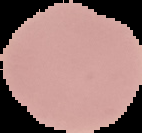 Result: no Plasmodium parasites seen. Segmented cell region on a black background. From a thin blood smear. Image is 142×133 pixels.